Describe the morphology of the red blood cells.
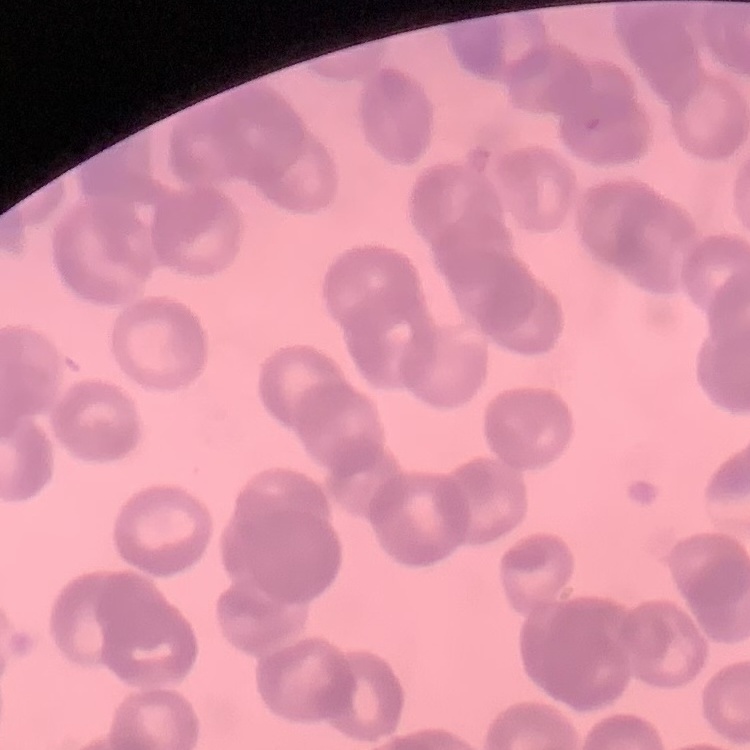
Rouleaux formation.

Thin blood film. Field's or Giemsa stain. Square crop of a larger photomicrograph.